Classify this cell by malaria status.
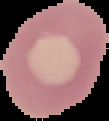
It is uninfected.

preparation = thin blood smear
image size = 109×121 pixels
image type = segmented cell region on a black background